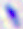

400x magnification. Toxoplasma gondii is shown. Micrograph.